Assess the morphology of the red blood cells.
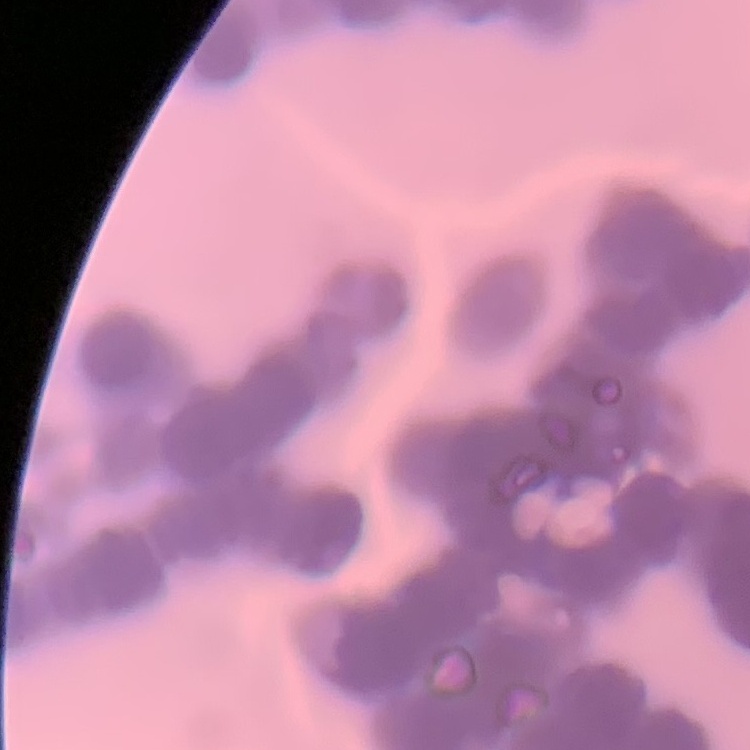

They show rouleaux formation.

image_type: square crop of a larger photomicrograph
stain: Field's or Giemsa
preparation: thin blood smear